Report the malaria status of this cell.
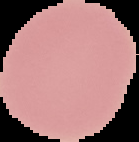

Uninfected.

The area outside the segmented cell region is set to black. From a thin blood film. Image is 139×142 pixels.